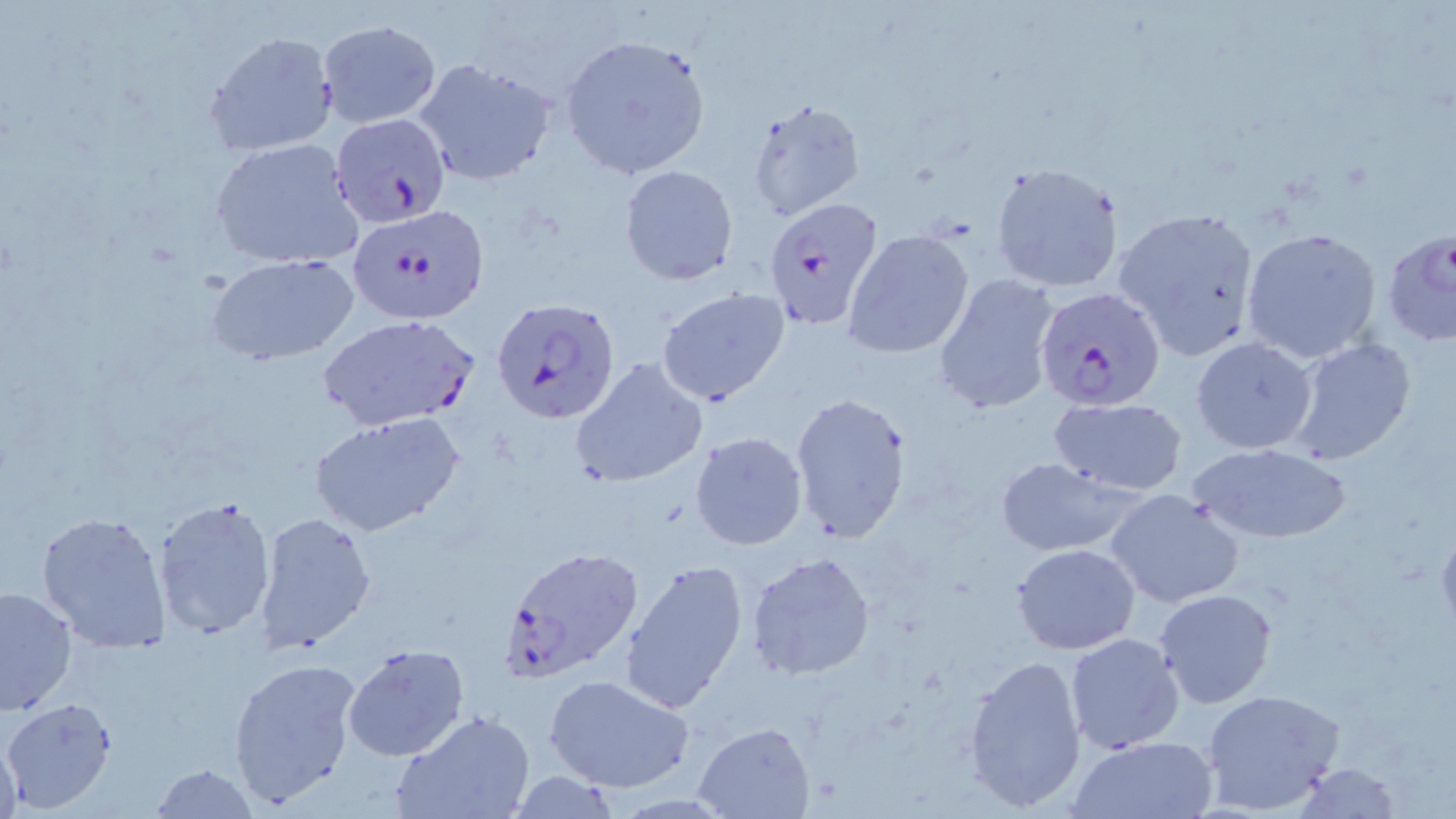

{
  "slide_level_diagnosis": "Plasmodium falciparum",
  "field_of_view": "one of a larger specimen",
  "image_size": "1456×819 pixels",
  "magnification": "1000x",
  "plasmodium_falciparum_infected_red_blood_cell_locations": "approximate bounding boxes as (x1,y1)-(x2,y2) corner pairs in pixels: (330,115)-(449,229), (761,200)-(885,332), (344,206)-(486,328), (1379,226)-(1456,347), (1031,293)-(1160,417), (492,302)-(622,429), (324,317)-(489,434), (498,551)-(645,689)",
  "modality": "optical microscopy",
  "stain": "May-Grünwald-Giemsa",
  "uninfected_red_blood_cell_locations": "approximate bounding boxes as (x1,y1)-(x2,y2) corner pairs in pixels: (317,18)-(441,128), (203,30)-(337,155), (560,34)-(712,180), (412,56)-(559,186), (744,98)-(867,222), (208,137)-(363,270), (988,162)-(1124,294), (619,164)-(738,286), (1119,207)-(1261,361), (1241,228)-(1386,364), (844,229)-(975,359), (206,252)-(360,364), (934,272)-(1062,415), (656,288)-(790,406), (1191,337)-(1319,454), (1288,337)-(1418,463), (572,358)-(708,489), (789,392)-(914,544), (1047,398)-(1188,494), (310,412)-(465,537), (689,431)-(809,551), (1185,441)-(1355,546), (994,457)-(1140,555), (1104,488)-(1246,609), (153,494)-(277,640), (36,509)-(170,652), (255,512)-(375,652), (1011,543)-(1139,654), (746,551)-(877,679), (619,560)-(748,715), (1,584)-(77,718), (1153,589)-(1279,708), (1064,631)-(1185,754), (342,644)-(470,762), (963,652)-(1088,814), (226,655)-(361,810), (543,671)-(696,794), (1200,687)-(1348,817), (3,699)-(116,812), (391,711)-(535,819), (692,722)-(816,818), (1,728)-(23,819), (1069,735)-(1216,818), (1290,762)-(1405,817), (146,763)-(259,818), (504,772)-(628,817)",
  "preparation": "thin blood film"
}